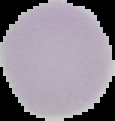
preparation = thin blood smear
image type = segmented cell region on a black background
result = negative for Plasmodium parasites
image size = 115×121 pixels